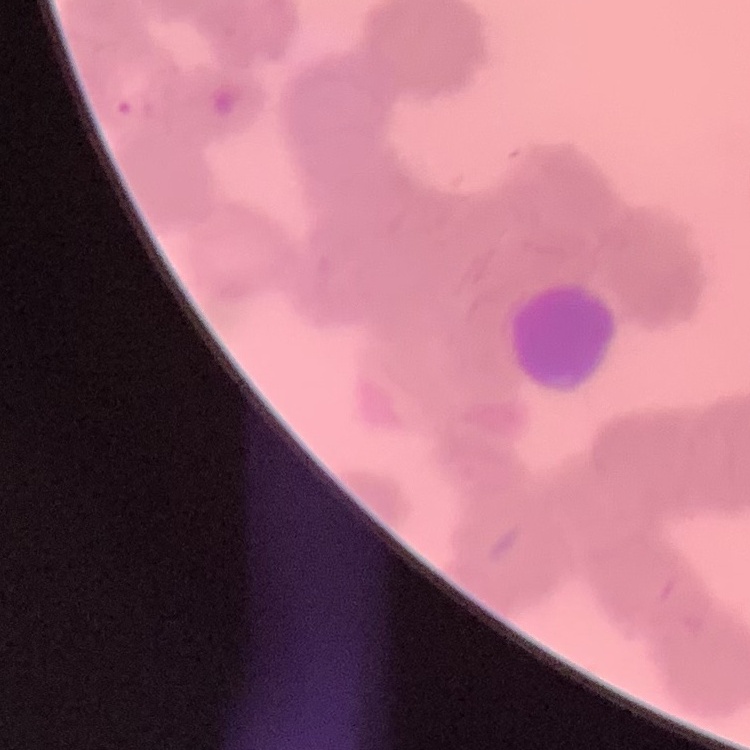

The red blood cells exhibit rouleaux formation. Thin blood smear. Square crop of a larger photomicrograph. Stained with either Field's or Giemsa.